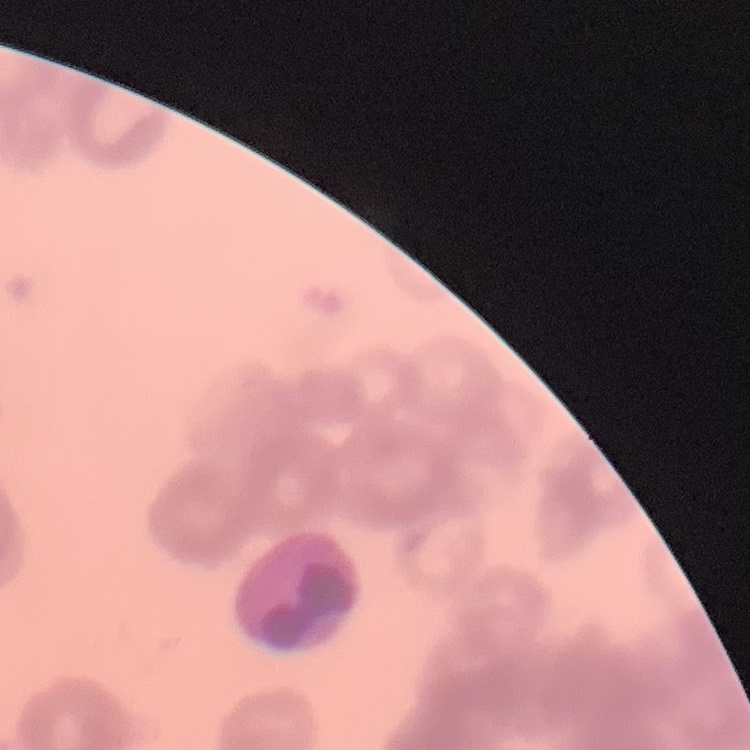

The red blood cells show rouleaux formation. Thin blood smear. One tile cut from a larger photomicrograph. Stained with either Field's or Giemsa.